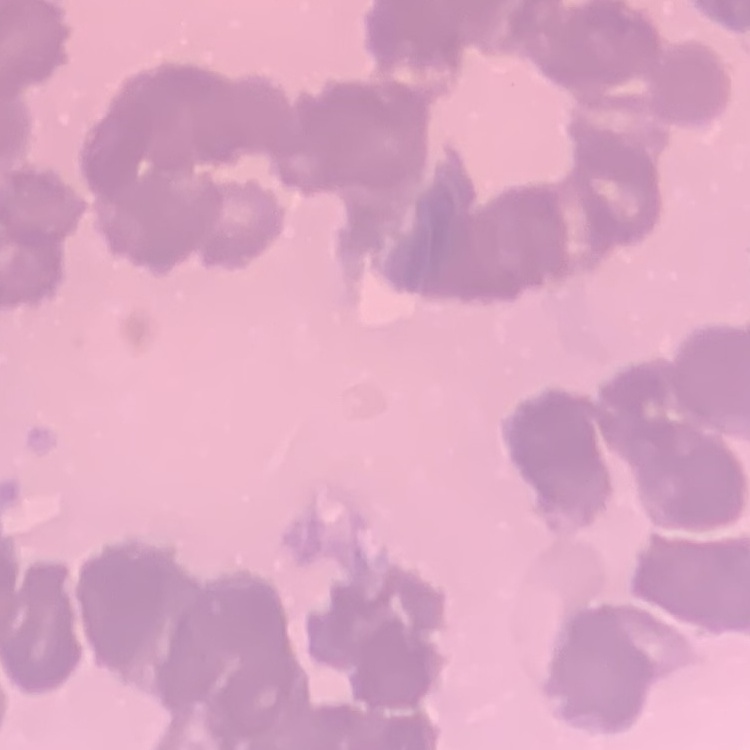

Summary:
  - Red blood cell morphology: rouleaux formation
  - Stain: Field's or Giemsa
  - Image type: square crop of a larger photomicrograph
  - Preparation: thin blood film